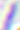
Micrograph. 400x magnification. Toxoplasma gondii is seen.